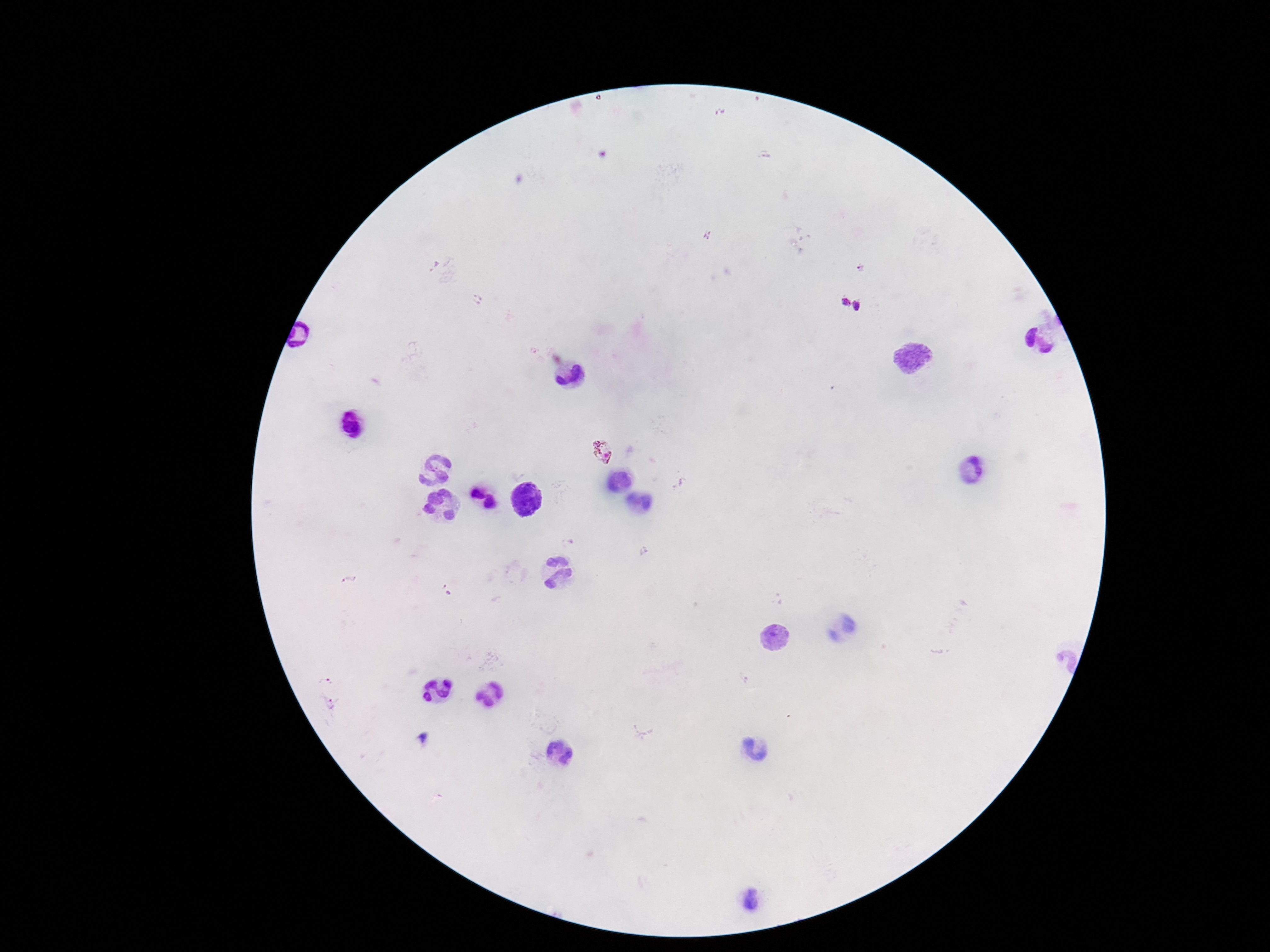 Approximate centers as {x, y} in pixels. Plasmodium parasite locations: {844, 303}, {859, 306}, {602, 450}. Photographed through the microscope eyepiece with a smartphone camera. One field from this slide. Patient malaria status: positive. Image is 1270×952 pixels. 100x magnification. Thick peripheral-blood smear. Giemsa stain.